State the blood parasite species.
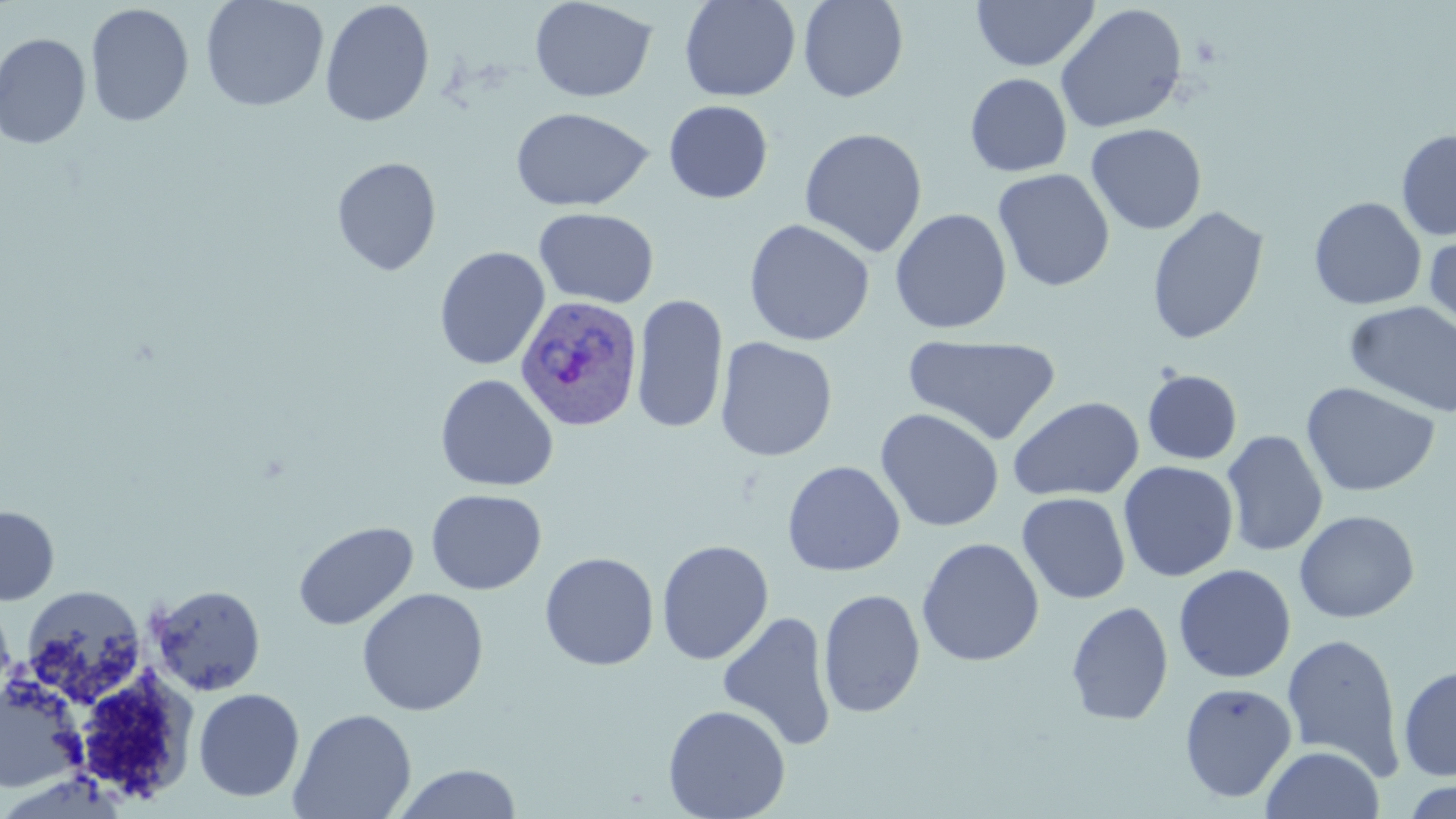

Plasmodium ovale.

Summary:
  - Coordinate format: approximate bounding boxes as [x1, y1, x2, y2] in pixels
  - Uninfected red blood cell locations: [200, 0, 329, 112], [529, 0, 658, 103], [679, 0, 801, 102], [797, 0, 909, 103], [971, 0, 1099, 71], [319, 1, 435, 128], [85, 3, 194, 128], [1054, 3, 1189, 133], [0, 32, 92, 149], [964, 72, 1072, 177], [663, 100, 773, 204], [510, 107, 652, 212], [1085, 122, 1207, 235], [799, 127, 928, 257], [1396, 128, 1456, 241], [331, 156, 442, 276], [992, 168, 1115, 292], [1308, 196, 1427, 310], [1146, 206, 1269, 344], [534, 207, 659, 309], [890, 208, 1012, 335], [743, 218, 875, 347], [1424, 228, 1456, 336], [434, 246, 550, 370], [631, 293, 729, 435], [1344, 300, 1456, 418], [902, 334, 1062, 446], [715, 336, 838, 462], [1142, 370, 1242, 465], [435, 374, 559, 492], [1301, 382, 1441, 497], [1007, 396, 1145, 501], [875, 407, 1005, 533], [1221, 430, 1328, 557], [782, 460, 905, 577], [1118, 460, 1239, 582], [1019, 485, 1239, 593], [426, 488, 547, 595], [1017, 492, 1131, 604], [1, 505, 59, 606], [1294, 510, 1420, 623], [293, 521, 418, 632], [916, 537, 1044, 667], [656, 539, 774, 666], [539, 551, 659, 671], [1173, 563, 1296, 683], [148, 584, 266, 696], [21, 585, 148, 706], [356, 588, 489, 716], [818, 589, 925, 718], [1066, 600, 1174, 726], [0, 602, 16, 704], [716, 610, 837, 751], [1281, 632, 1407, 780], [1397, 664, 1456, 781], [71, 668, 197, 803], [0, 678, 82, 794], [1178, 682, 1298, 803], [193, 688, 305, 802], [662, 704, 791, 818], [289, 708, 417, 819], [1260, 744, 1385, 819], [391, 763, 523, 819], [1399, 778, 1456, 818]
  - Plasmodium ovale-infected red blood cell locations: [514, 294, 644, 432]
  - Stain: May-Grünwald-Giemsa
  - Magnification: 1000x
  - Field of view: single
  - Preparation: thin blood film
  - Modality: optical microscopy
  - Image size: 1456×819 pixels